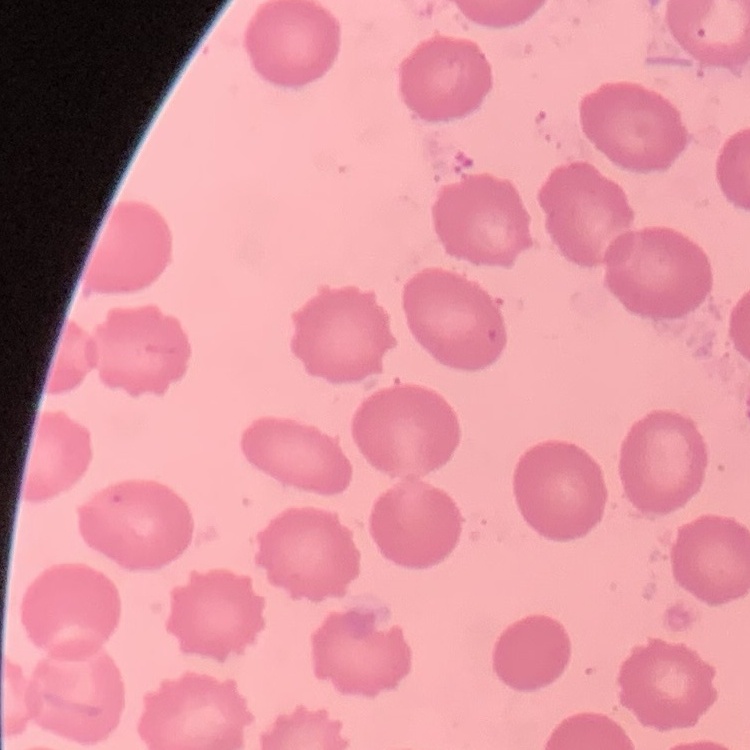
Summary:
  - Red blood cell morphology: no rouleaux formation
  - Preparation: thin peripheral smear
  - Stain: Field's or Giemsa
  - Image type: one tile cut from a larger photomicrograph